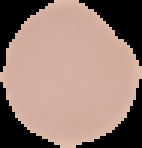

Summary:
  - Image size: 142×148 pixels
  - Result: no Plasmodium parasites seen
  - Image type: segmented cell region with the area outside set to black
  - Preparation: thin blood film